Locate and identify every blood parasite.
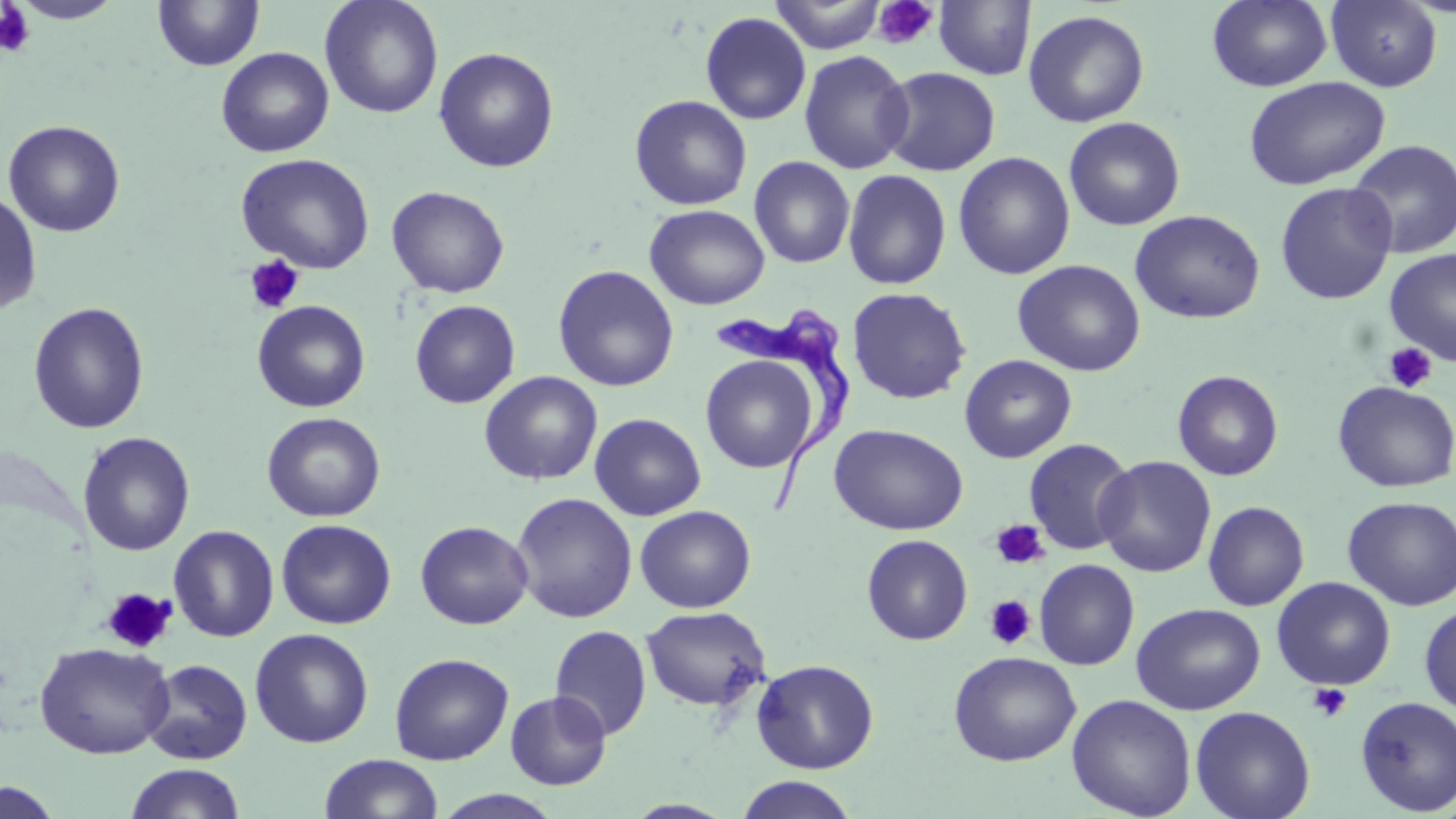
Approximate bounding boxes as (x1, y1, x2, y2) in pixels.
Trypanosoma brucei: (712, 310, 854, 520).
No Plasmodium falciparum, Plasmodium ovale, Plasmodium malariae, Plasmodium vivax, or Babesia divergens observed.

Summary:
  - Uninfected red blood cell locations: (152, 0, 265, 72), (320, 0, 443, 119), (768, 0, 889, 54), (1207, 0, 1332, 91), (1325, 0, 1443, 92), (12, 1, 124, 24), (933, 1, 1036, 80), (1023, 9, 1150, 128), (700, 12, 812, 125), (216, 47, 334, 158), (434, 47, 560, 173), (798, 50, 915, 174), (880, 66, 1000, 176), (1243, 76, 1390, 190), (630, 95, 752, 211), (1063, 116, 1186, 231), (3, 120, 126, 237), (1346, 138, 1456, 259), (953, 152, 1075, 279), (236, 153, 375, 274), (749, 156, 855, 268), (842, 169, 951, 290), (1274, 181, 1398, 306), (387, 186, 509, 298), (0, 188, 42, 317), (645, 204, 770, 310), (1130, 209, 1266, 324), (1384, 248, 1456, 366), (1012, 259, 1146, 376), (553, 265, 679, 392), (847, 287, 972, 405), (252, 300, 371, 413), (410, 300, 520, 409), (28, 302, 150, 434), (699, 354, 820, 473), (959, 354, 1077, 463), (1172, 370, 1284, 481), (479, 371, 603, 486), (1332, 380, 1456, 493), (261, 412, 387, 522), (589, 413, 706, 521), (829, 423, 969, 535), (77, 431, 196, 556), (1023, 438, 1136, 555), (1095, 456, 1216, 577), (511, 492, 638, 623), (1342, 495, 1456, 611), (1203, 501, 1309, 611), (635, 505, 757, 613), (276, 518, 396, 629), (415, 520, 534, 629), (169, 524, 279, 642), (861, 534, 973, 645), (1034, 558, 1140, 670), (1271, 576, 1396, 691), (1131, 602, 1266, 715), (1419, 602, 1456, 715), (640, 605, 771, 712), (550, 624, 652, 741), (249, 628, 374, 748), (35, 641, 175, 759), (948, 650, 1082, 766), (389, 652, 514, 764), (141, 659, 253, 764), (751, 659, 879, 774), (505, 690, 612, 790), (1066, 694, 1197, 819), (1355, 696, 1456, 816), (1190, 705, 1316, 819), (319, 753, 443, 819), (124, 763, 248, 819), (734, 775, 859, 818), (1, 780, 66, 819), (432, 789, 566, 818)
  - Platelet locations: (871, 0, 939, 50), (0, 3, 35, 57), (243, 254, 305, 315), (1383, 341, 1437, 393), (990, 519, 1049, 570), (101, 587, 177, 654), (984, 594, 1036, 649), (1308, 683, 1352, 723)
  - Slide-level diagnosis: Trypanosoma brucei
  - Magnification: 1000x
  - Field of view: one of a larger specimen
  - Stain: May-Grünwald-Giemsa
  - Preparation: thin blood film
  - Image size: 1456×819 pixels
  - Modality: light microscopy